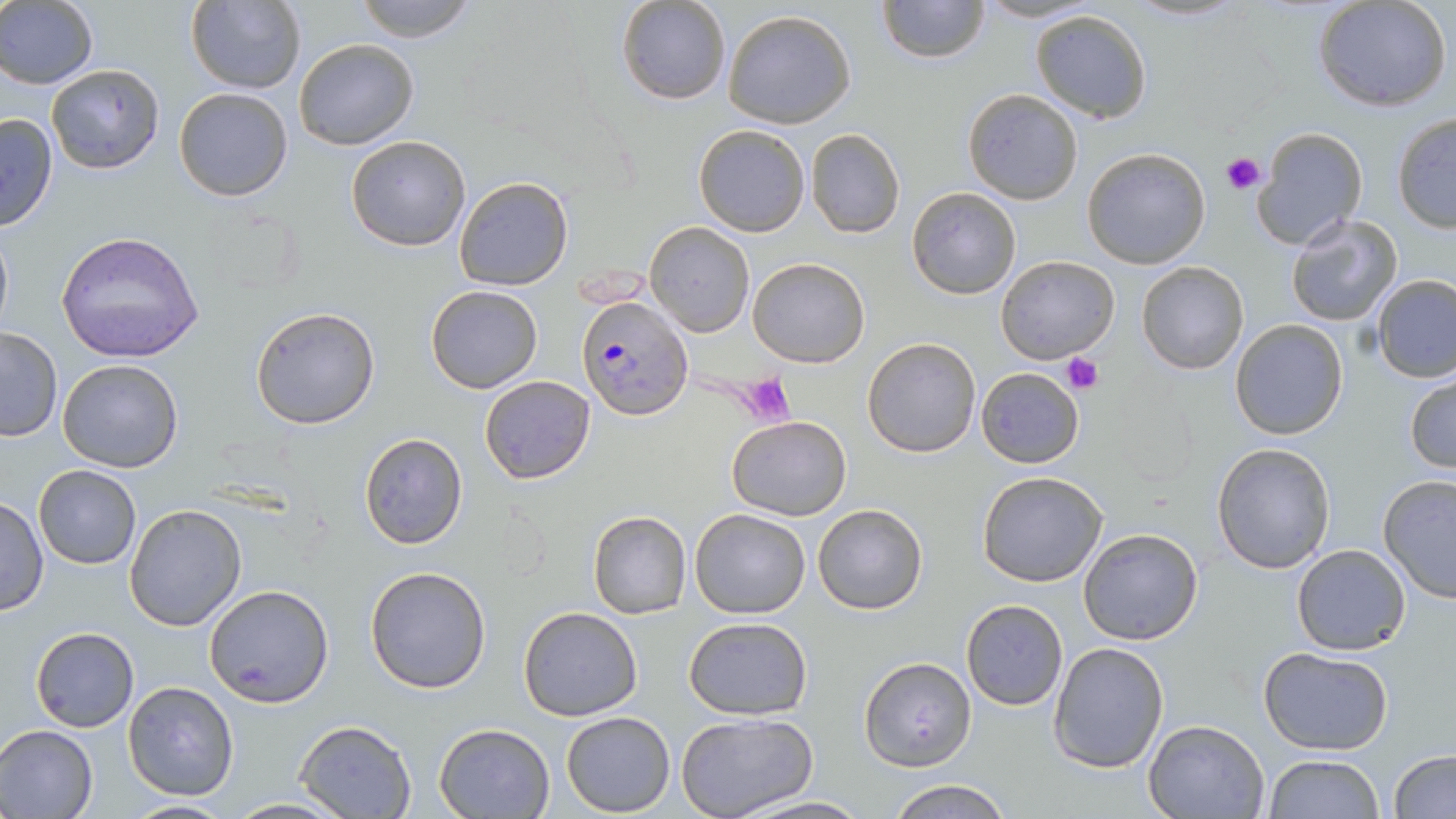
Approximate bounding boxes as (x1, y1, x2, y2) in pixels. Platelet locations: (1221, 151, 1265, 195), (1063, 351, 1103, 395), (737, 374, 795, 427). Plasmodium falciparum-infected red blood cell locations: (578, 294, 693, 419). Uninfected red blood cell locations: (186, 0, 305, 94), (354, 0, 477, 42), (616, 0, 732, 105), (877, 0, 989, 64), (1125, 0, 1252, 23), (1313, 1, 1453, 113), (0, 2, 99, 88), (722, 9, 857, 129), (1030, 10, 1152, 124), (294, 37, 419, 150), (45, 64, 164, 175), (175, 86, 293, 202), (962, 89, 1083, 205), (0, 112, 58, 233), (1391, 113, 1456, 233), (693, 124, 810, 237), (1251, 126, 1367, 250), (806, 128, 905, 239), (346, 135, 471, 253), (1083, 147, 1210, 269), (454, 175, 574, 291), (907, 186, 1021, 300), (1283, 214, 1404, 328), (0, 221, 13, 343), (644, 221, 754, 336), (55, 231, 206, 364), (996, 254, 1119, 365), (747, 257, 871, 368), (1137, 261, 1250, 375), (1371, 275, 1456, 382), (426, 285, 543, 394), (250, 306, 381, 429), (1229, 318, 1348, 439), (0, 328, 62, 440), (863, 337, 980, 457), (56, 358, 184, 473), (975, 366, 1085, 467), (1405, 371, 1456, 477), (479, 375, 596, 484), (1113, 390, 1203, 489), (717, 413, 834, 612), (728, 415, 852, 521), (360, 433, 467, 548), (1211, 442, 1336, 575), (34, 467, 141, 568), (976, 470, 1110, 587), (1377, 474, 1456, 603), (1, 496, 48, 616), (124, 502, 248, 632), (812, 502, 929, 615), (690, 508, 811, 619), (587, 509, 692, 620), (1077, 528, 1203, 645), (1290, 544, 1413, 657), (365, 566, 492, 694), (205, 583, 336, 707), (959, 599, 1069, 711), (518, 606, 644, 722), (684, 616, 812, 719), (30, 627, 139, 732), (1047, 641, 1170, 774), (1258, 646, 1393, 754), (860, 655, 977, 771), (121, 680, 240, 801), (559, 712, 675, 816), (675, 713, 818, 819), (1143, 718, 1271, 818), (293, 719, 418, 818), (433, 723, 555, 817), (0, 725, 99, 817), (1387, 749, 1456, 819), (1262, 754, 1384, 818), (887, 778, 1014, 818), (738, 795, 871, 817), (225, 798, 351, 817), (118, 799, 238, 816). Slide-level diagnosis: Plasmodium falciparum. Image is 1456×819 pixels. Captured at 1000x magnification. Thin blood smear. Light microscopy. May-Grünwald-Giemsa-stained preparation. One field of a larger specimen.